Assess this cell for malaria.
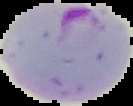
Parasitized.

Segmented cell region on a black background. Image is 133×106 pixels. From a thin blood smear.